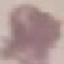
Summary:
  - Malaria status: uninfected
  - Capture: smartphone through the microscope eyepiece
  - Stain: Giemsa
  - Preparation: thin smear
  - Image type: cell patch, automatically extracted from a larger field of view and resized to 64 × 64 pixels